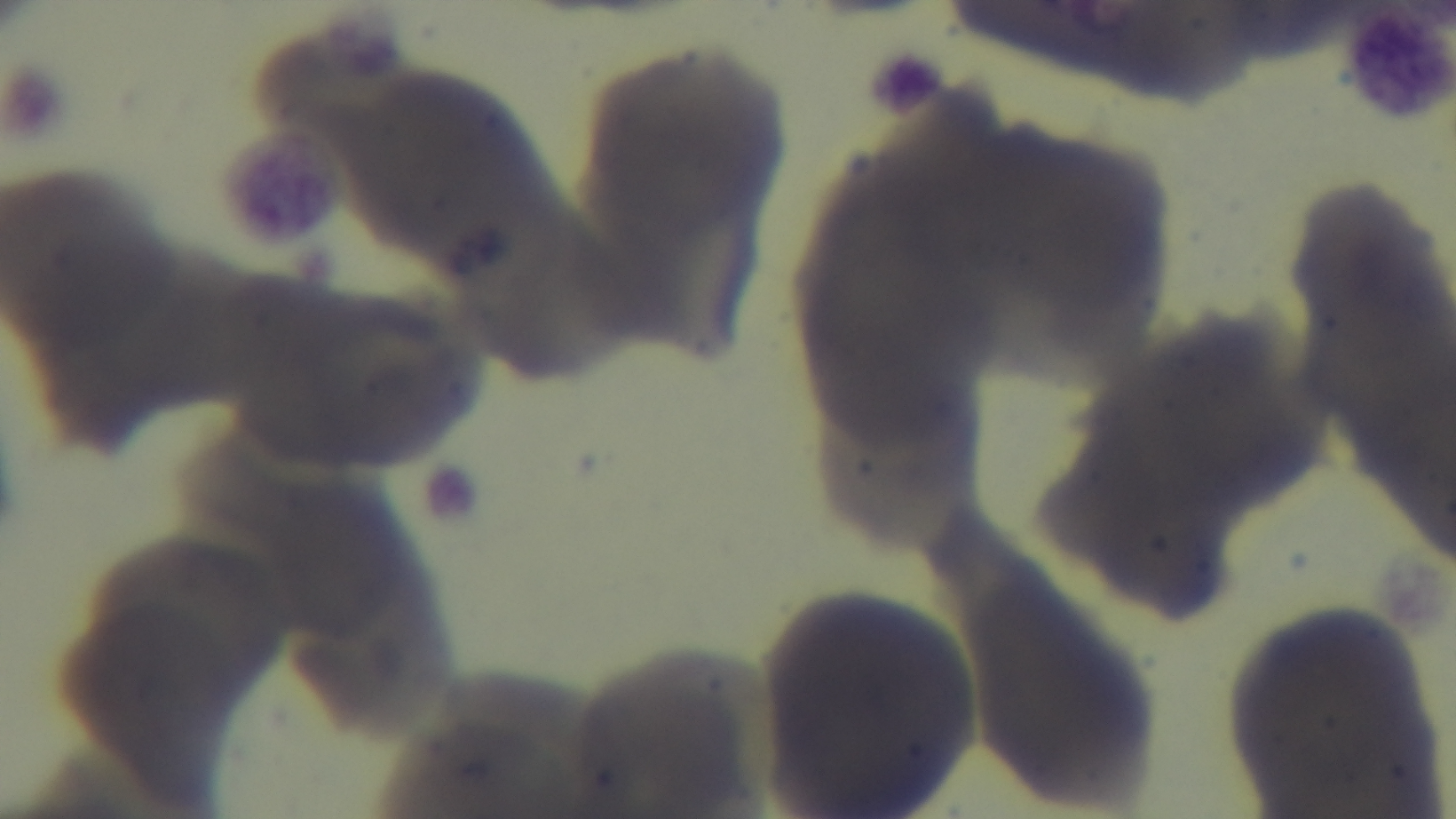

Summary:
  - Stain: Giemsa
  - Modality: light microscopy
  - Capture: mounted 4K digital camera
  - Field of view: single
  - Objective: 100x oil immersion
  - Preparation: thin blood film
  - Malaria status: uninfected